Outline each uninfected red blood cell.
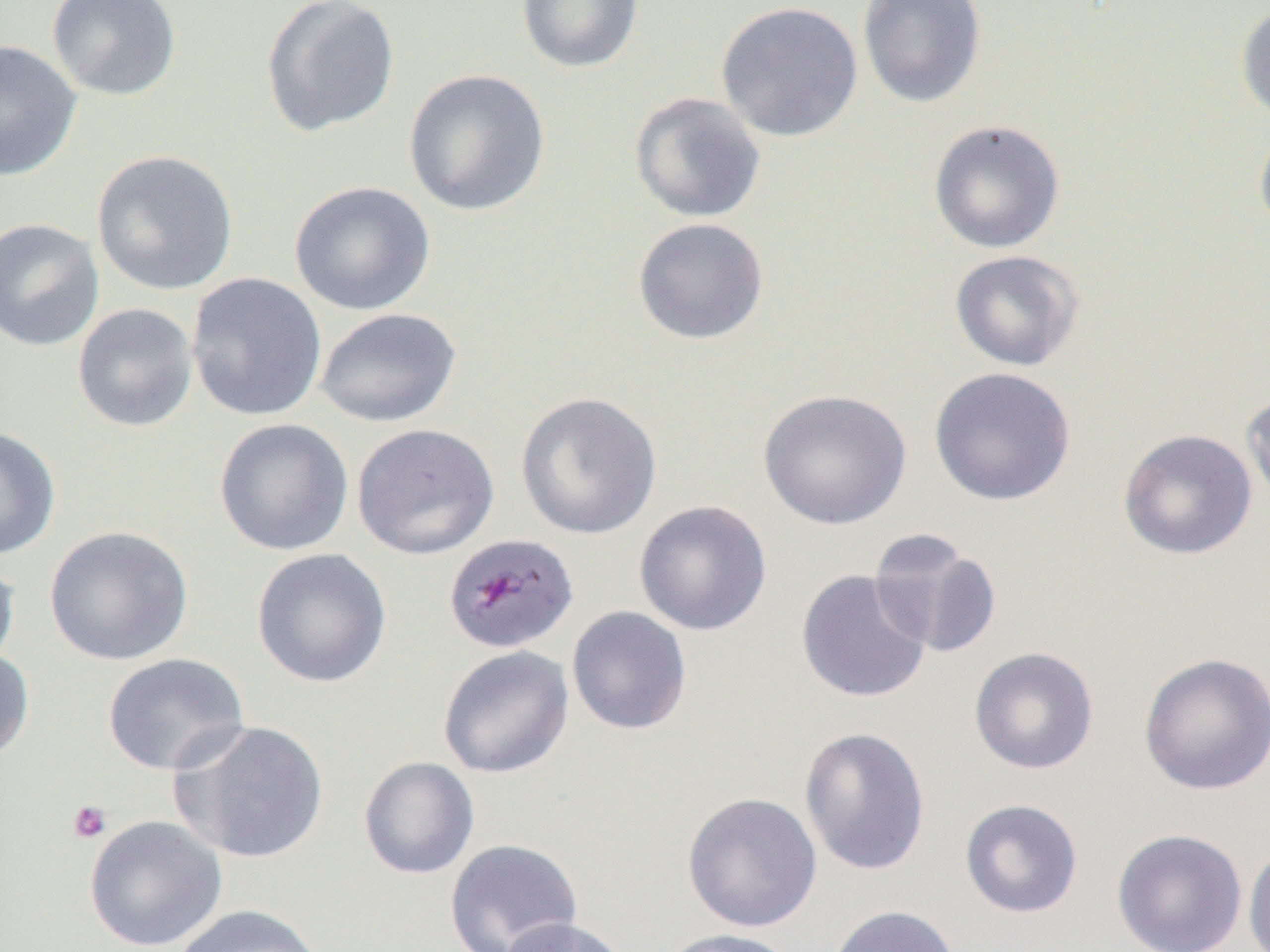

Approximate bounding boxes as (x1, y1, x2, y2) in pixels.
Uninfected red blood cells: (45, 0, 182, 101), (260, 0, 400, 138), (515, 0, 644, 74), (858, 0, 986, 108), (715, 1, 864, 142), (1236, 4, 1270, 124), (0, 39, 81, 182), (403, 69, 550, 217), (630, 91, 766, 223), (1254, 117, 1270, 238), (928, 119, 1066, 254), (91, 149, 239, 296), (289, 180, 436, 316), (0, 217, 104, 352), (633, 217, 769, 345), (948, 249, 1084, 372), (186, 273, 327, 421), (72, 303, 198, 432), (315, 307, 461, 427), (928, 367, 1077, 506), (757, 388, 912, 530), (1242, 389, 1270, 511), (515, 390, 663, 540), (214, 418, 353, 556), (351, 423, 500, 560), (0, 426, 60, 560), (1118, 428, 1258, 561), (634, 500, 772, 636), (44, 525, 193, 666), (868, 529, 1003, 661), (251, 548, 392, 688), (0, 552, 20, 674), (795, 569, 933, 704), (566, 606, 692, 735), (437, 645, 574, 779), (0, 646, 35, 763), (969, 646, 1099, 775), (1138, 652, 1270, 795), (102, 653, 250, 776), (169, 719, 330, 864), (799, 726, 930, 876), (358, 756, 479, 880), (681, 791, 822, 933), (959, 799, 1083, 919), (84, 815, 227, 952), (1111, 828, 1248, 952), (443, 838, 583, 952), (1242, 840, 1270, 952), (173, 904, 324, 952), (826, 905, 961, 952), (496, 916, 633, 952), (657, 927, 800, 952).

Platelet locations: (66, 800, 111, 843). Plasmodium malariae-infected red blood cell locations: (444, 533, 578, 654). Slide-level diagnosis: Plasmodium malariae. Thin blood smear. Captured at 1000x magnification. One field of a larger specimen. Optical microscopy. Image is 1270×952 pixels.